Report the malaria status of this cell.
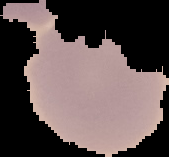

Uninfected.

image size = 169×157 pixels
image type = segmented cell region with the area outside set to black
preparation = thin blood smear